Name the parasite shown.
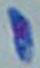

Toxoplasma gondii.

1000x magnification. Micrograph.